Report the malaria status of this cell.
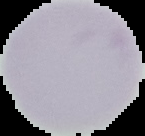
It is uninfected.

Image is 145×136 pixels. Cell region segmented out of the field of view; the surrounding area is masked to black. From a thin blood smear.